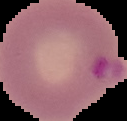

Summary:
  - Preparation: thin blood smear
  - Image type: segmented cell region on a black background
  - Image size: 127×121 pixels
  - Result: malaria parasites identified